Locate and identify every blood parasite.
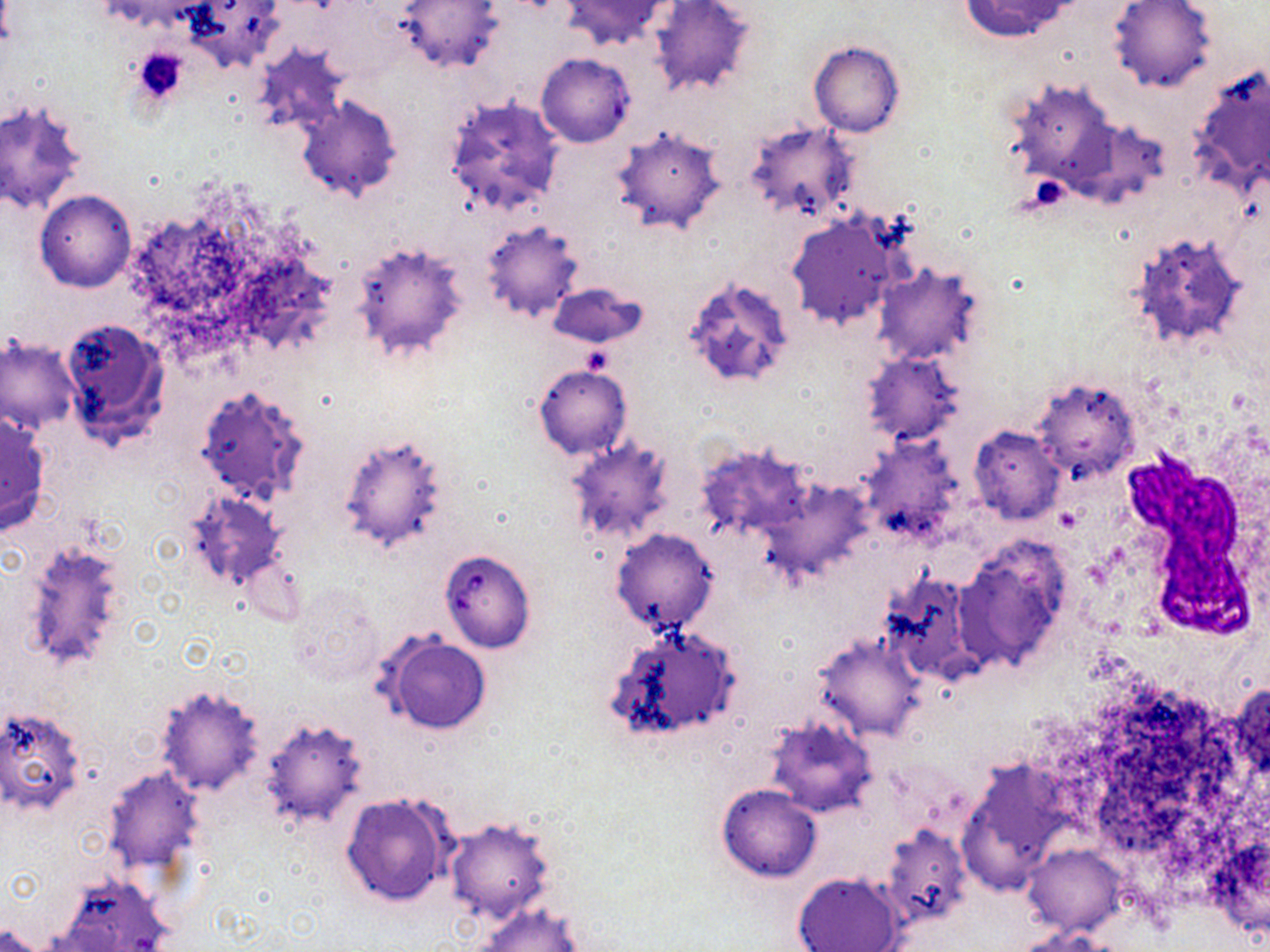
Approximate bounding boxes as (x1,y1)-(x2,y2) corner pairs in pixels.
Babesia divergens-infected red blood cells: (440,550)-(537,652).
No Plasmodium falciparum, Plasmodium ovale, Plasmodium malariae, Plasmodium vivax, or Trypanosoma brucei observed.

Summary:
  - Platelet locations: (132,47)-(191,105)
  - Uninfected red blood cell locations: (186,0)-(286,70), (396,0)-(503,73), (561,0)-(671,49), (960,0)-(1074,41), (1109,0)-(1218,93), (651,2)-(760,98), (809,42)-(904,137), (251,45)-(348,139), (1185,63)-(1269,192), (295,95)-(402,202), (440,95)-(567,219), (1,98)-(90,214), (744,120)-(861,225), (612,127)-(727,235), (35,190)-(137,292), (786,211)-(906,332), (479,222)-(584,323), (1125,229)-(1254,355), (348,237)-(472,364), (873,264)-(987,367), (680,275)-(798,392), (548,283)-(647,347), (60,317)-(171,451), (1,335)-(80,434), (861,351)-(964,446), (534,365)-(632,458), (1030,375)-(1140,479), (191,383)-(310,504), (0,410)-(52,535), (967,425)-(1067,524), (337,433)-(453,554), (562,437)-(677,547), (857,437)-(963,546), (697,444)-(813,539), (768,479)-(873,579), (182,489)-(292,596), (611,528)-(718,635), (16,536)-(133,677), (953,537)-(1076,674), (879,570)-(981,682), (283,580)-(386,689), (604,623)-(744,745), (813,634)-(926,741), (381,636)-(491,736), (155,682)-(266,796), (1,706)-(88,817), (258,715)-(368,829), (762,717)-(875,817), (958,757)-(1073,892), (102,765)-(205,873), (716,783)-(822,882), (339,793)-(455,908), (444,815)-(558,925), (1202,826)-(1269,944), (1021,843)-(1127,937), (52,872)-(172,952), (791,872)-(906,952), (471,901)-(584,952), (0,925)-(48,952), (1017,926)-(1119,952)
  - White blood cell locations: (1122,457)-(1259,640)
  - Slide-level diagnosis: Babesia divergens
  - Preparation: thin blood smear
  - Magnification: 1000x
  - Image size: 1270×952 pixels
  - Field of view: single
  - Stain: May-Grünwald-Giemsa
  - Modality: optical microscopy